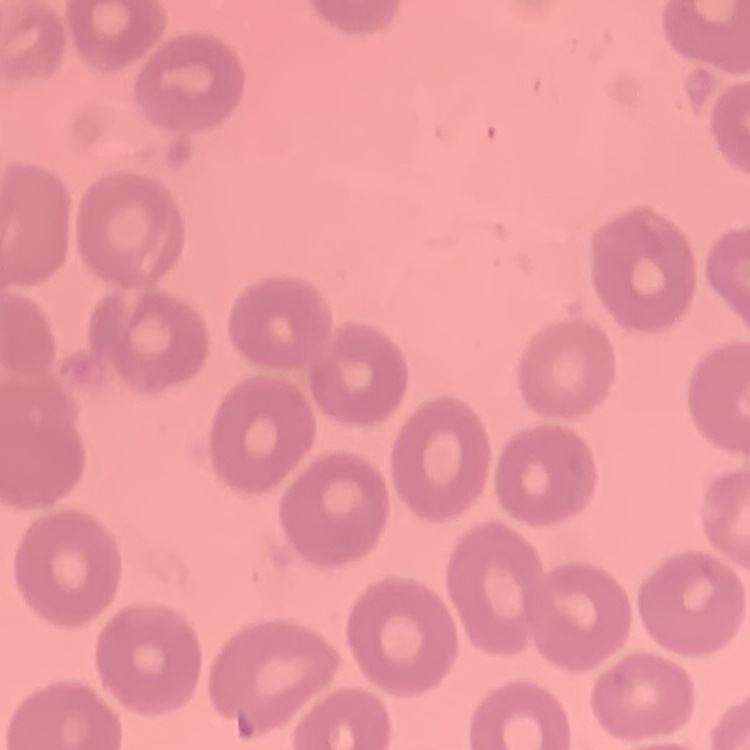 The red blood cells show no rouleaux formation. Square crop of a larger photomicrograph. Stained with either Field's or Giemsa. Thin peripheral smear.